Assess this cell for malaria.
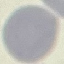
Uninfected.

Photographed with a smartphone camera at the microscope eyepiece. Giemsa stain. Thin smear of blood. Automatically extracted cell patch, resized to 64 × 64 pixels.